Look for Plasmodium parasites.
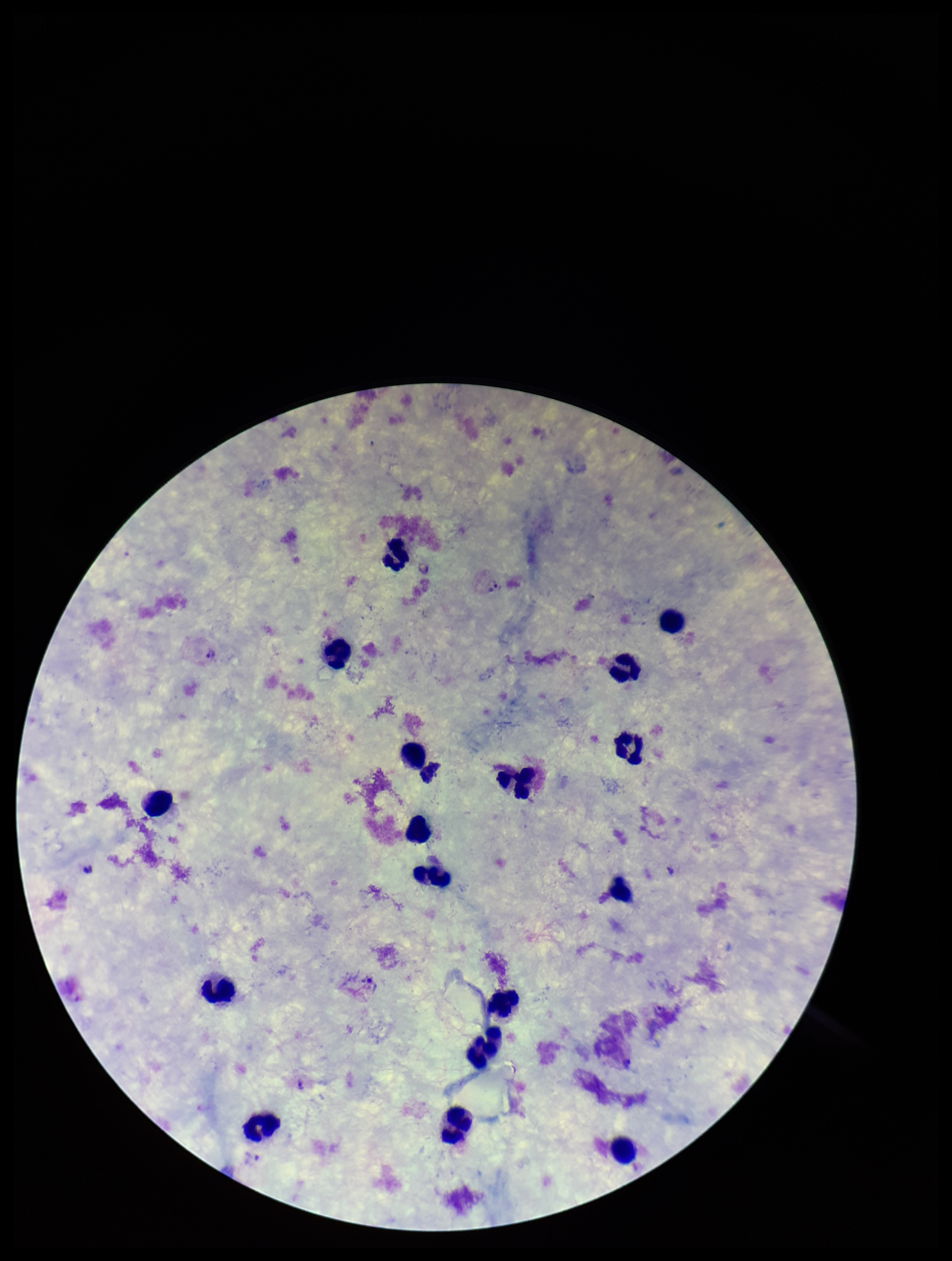
Detected.

Single field of view. Species reported for this patient: Plasmodium vivax. Parasite count: 2. Patient malaria status: infected. Image is 952×1261 pixels. Preparation: thick blood smear. Leukocyte count: 17. Giemsa stain. Smartphone photograph taken through the eyepiece of a microscope.